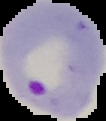
Summary:
  - Malaria status: parasitized
  - Image size: 106×121 pixels
  - Image type: segmented cell region with the area outside set to black
  - Preparation: thin blood film